Classify this cell by malaria status.
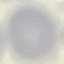
Uninfected.

image type = cell patch, automatically extracted from a larger field of view and resized to 64 × 64 pixels
capture = smartphone camera at the microscope eyepiece
stain = Giemsa
preparation = thin blood smear